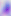

Summary:
  - Magnification: 400x
  - Modality: micrograph
  - Identification: Toxoplasma gondii